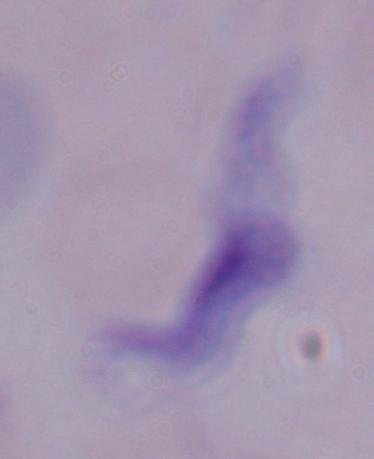

A trypanosome is shown. Photomicrograph. Captured at 1000x magnification.